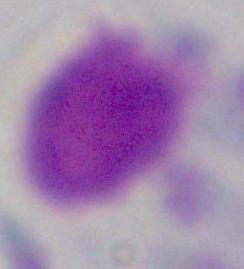

Photomicrograph. A leukocyte is shown. 1000x magnification.